Assess the morphology of the red blood cells.
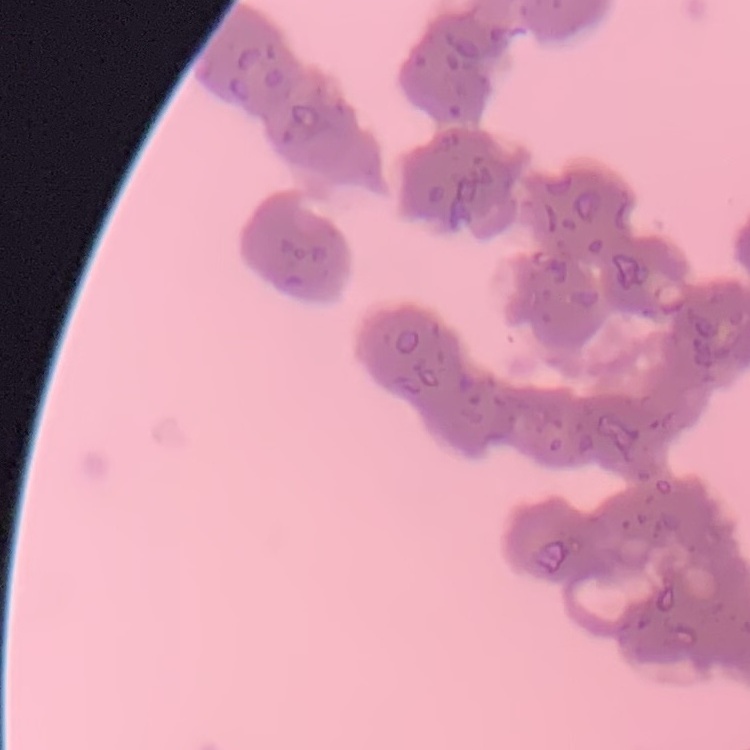

They show rouleaux formation.

Summary:
  - Stain: Field's or Giemsa
  - Image type: one tile cut from a larger photomicrograph
  - Preparation: thin blood smear